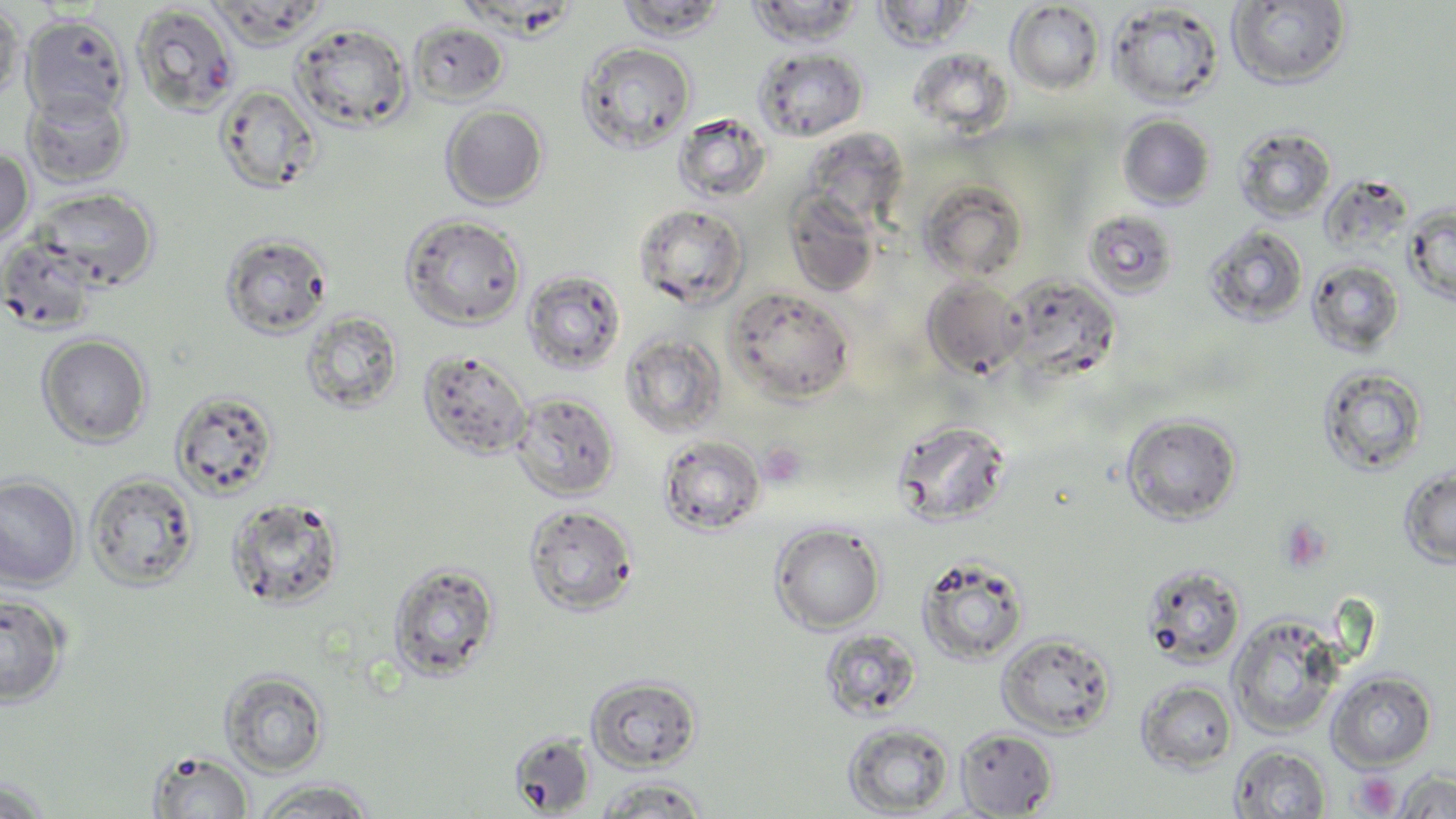

Summary:
  - Coordinate format: approximate bounding boxes as (x1, y1, x2, y2) in pixels
  - Platelet locations: (759, 440, 809, 488), (1278, 518, 1333, 575), (1351, 771, 1400, 816)
  - Uninfected red blood cell locations: (616, 0, 728, 41), (1226, 0, 1352, 89), (747, 1, 863, 46), (871, 1, 975, 51), (0, 2, 25, 104), (1005, 2, 1104, 95), (1108, 2, 1225, 108), (130, 4, 240, 118), (20, 14, 130, 122), (291, 21, 413, 132), (408, 21, 509, 105), (577, 41, 697, 154), (754, 47, 868, 141), (908, 47, 1010, 135), (214, 84, 323, 196), (22, 88, 132, 187), (441, 104, 548, 208), (672, 113, 771, 204), (1119, 115, 1215, 209), (1233, 125, 1336, 224), (800, 128, 910, 230), (0, 148, 35, 245), (1322, 170, 1422, 257), (918, 179, 1029, 283), (32, 187, 159, 290), (785, 191, 881, 297), (633, 203, 749, 309), (1403, 204, 1456, 307), (1082, 210, 1179, 299), (401, 213, 527, 330), (1204, 225, 1309, 327), (220, 231, 333, 340), (0, 233, 103, 334), (1306, 260, 1405, 356), (521, 269, 626, 376), (1005, 274, 1122, 381), (921, 277, 1029, 379), (726, 287, 856, 405), (300, 310, 404, 414), (36, 333, 152, 448), (622, 333, 728, 438), (417, 349, 533, 461), (1317, 366, 1428, 476), (170, 389, 279, 500), (509, 391, 621, 502), (1120, 413, 1242, 525), (890, 417, 1014, 528), (657, 434, 766, 535), (1398, 468, 1456, 569), (85, 472, 200, 590), (0, 475, 82, 589), (225, 495, 346, 611), (523, 503, 639, 617), (770, 522, 886, 634), (916, 554, 1031, 666), (387, 560, 501, 682), (1140, 563, 1246, 669), (0, 592, 70, 708), (1227, 613, 1345, 738), (818, 628, 922, 722), (997, 632, 1117, 738), (221, 669, 329, 776), (1327, 670, 1437, 770), (587, 674, 702, 772), (1136, 680, 1237, 774), (843, 722, 954, 816), (954, 727, 1059, 818), (509, 732, 596, 816), (1229, 744, 1331, 817), (148, 750, 255, 819), (1394, 769, 1456, 818), (593, 776, 711, 818), (1, 778, 55, 818), (251, 779, 380, 817)
  - Slide-level diagnosis: negative for blood parasites
  - Field of view: single
  - Preparation: thin blood film
  - Magnification: 1000x
  - Image size: 1456×819 pixels
  - Stain: May-Grünwald-Giemsa
  - Modality: light microscopy